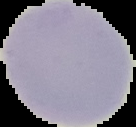

Summary:
  - Preparation: thin blood smear
  - Image size: 136×127 pixels
  - Image type: segmented cell region with the area outside set to black
  - Malaria status: uninfected